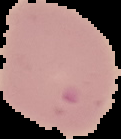

Cell region segmented out of the field of view; the surrounding area is masked to black. From a thin blood film. Image is 121×139 pixels. Malaria status: parasitized.